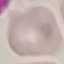
Result: no malaria parasites detected. Thin blood film. Automatically extracted cell patch, resized to 64 × 64 pixels. Giemsa stain. Photographed with a smartphone camera at the microscope eyepiece.